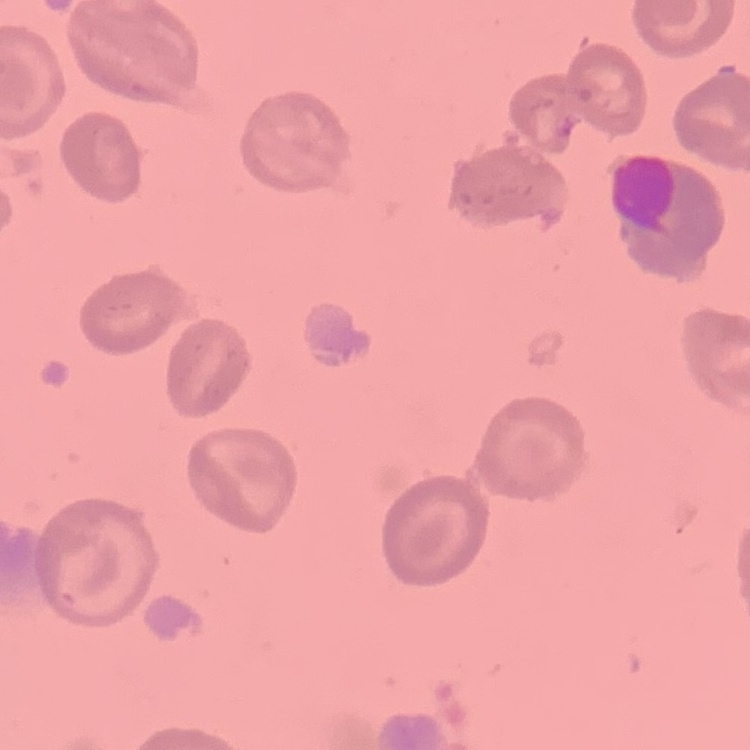
The erythrocytes show no rouleaux formation. Thin blood smear. Stained with either Field's or Giemsa. Square crop of a larger photomicrograph.